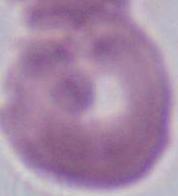

A red blood cell is shown. 1000x magnification. Photomicrograph.